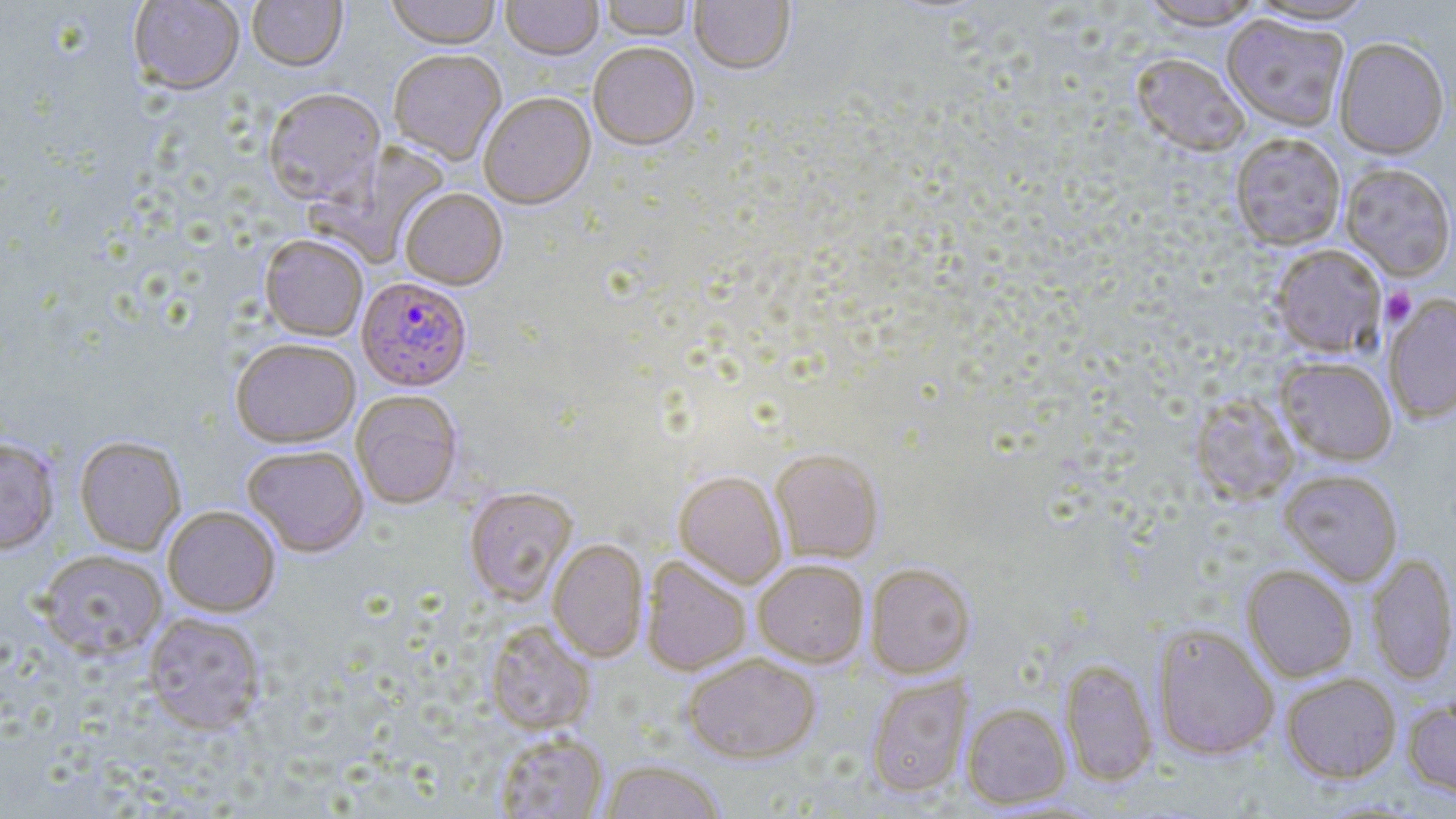

Summary:
  - Coordinate format: approximate bounding boxes as (x1, y1, x2, y2) in pixels
  - Uninfected red blood cell locations: (128, 0, 245, 96), (247, 0, 347, 74), (385, 0, 501, 53), (501, 0, 603, 63), (600, 0, 693, 43), (690, 0, 795, 77), (1137, 0, 1266, 29), (1245, 0, 1381, 25), (1221, 14, 1349, 132), (1334, 36, 1450, 159), (588, 45, 700, 153), (388, 52, 506, 167), (1131, 52, 1250, 157), (262, 90, 386, 209), (479, 95, 596, 213), (1230, 132, 1346, 250), (309, 143, 451, 268), (1340, 162, 1456, 280), (399, 190, 508, 292), (260, 236, 368, 342), (1269, 244, 1387, 358), (1383, 294, 1456, 424), (230, 340, 361, 450), (1276, 356, 1397, 465), (351, 392, 463, 509), (1190, 392, 1300, 505), (74, 436, 186, 555), (0, 437, 60, 554), (243, 446, 369, 558), (770, 450, 884, 564), (1280, 469, 1403, 586), (673, 472, 787, 589), (464, 488, 578, 606), (163, 506, 280, 617), (547, 540, 648, 663), (37, 549, 167, 659), (1366, 553, 1456, 686), (641, 557, 752, 676), (753, 560, 869, 668), (865, 564, 976, 678), (1241, 565, 1358, 682), (143, 612, 266, 734), (485, 622, 596, 735), (1151, 622, 1279, 761), (683, 655, 821, 764), (1059, 658, 1158, 786), (1281, 672, 1401, 783), (866, 675, 972, 798), (1402, 696, 1456, 798), (962, 703, 1071, 809), (493, 732, 609, 818), (600, 760, 726, 819)
  - Plasmodium falciparum-infected red blood cell locations: (356, 278, 472, 393)
  - Platelet locations: (1381, 288, 1417, 327)
  - Slide-level diagnosis: Plasmodium falciparum
  - Stain: May-Grünwald-Giemsa
  - Modality: optical microscopy
  - Image size: 1456×819 pixels
  - Magnification: 1000x
  - Preparation: thin blood film
  - Field of view: single